Name the cell type shown.
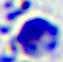

This is a leukocyte.

Summary:
  - Modality: micrograph
  - Magnification: 400x